Locate Plasmodium parasites and leukocytes.
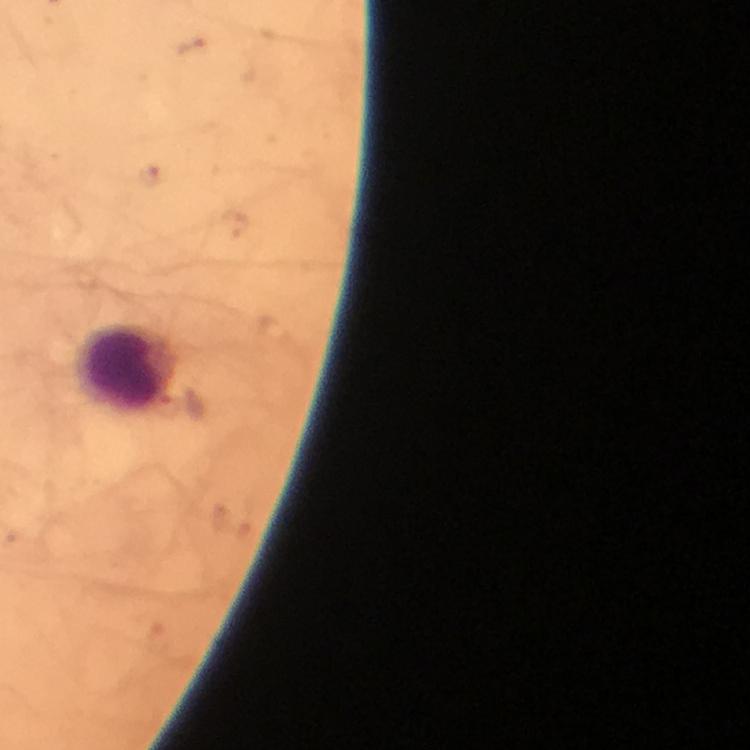

No Plasmodium parasites seen.
Approximate centers as (x, y) in pixels.
Leukocytes: (128, 368).

capture = smartphone mounted on the microscope
stain = Giemsa
cropped from = a single field of view
context = from a diagnostic examination for malaria
preparation = thick blood smear
magnification = 100x
immersion oil = used
image size = 750×750 pixels